Identify the cell.
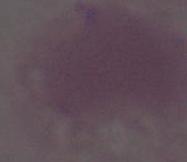
An erythrocyte.

{
  "magnification": "1000x",
  "modality": "micrograph"
}